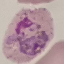
malaria status = uninfected
preparation = thin smear
image type = cell patch, automatically extracted from a larger field of view and resized to 64 × 64 pixels
capture = smartphone through the microscope eyepiece
stain = Giemsa